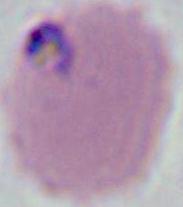

Summary:
  - Identification: Plasmodium
  - Modality: photomicrograph
  - Magnification: 400x or 1000x